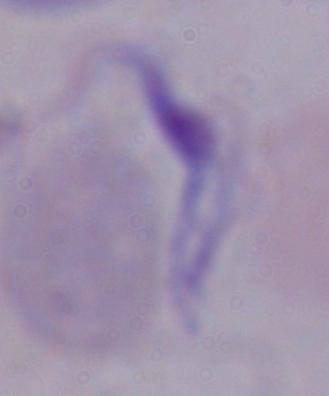
modality = micrograph
identification = trypanosome
magnification = 1000x